Give the position of every P. falciparum parasite, noting its life-cycle stage.
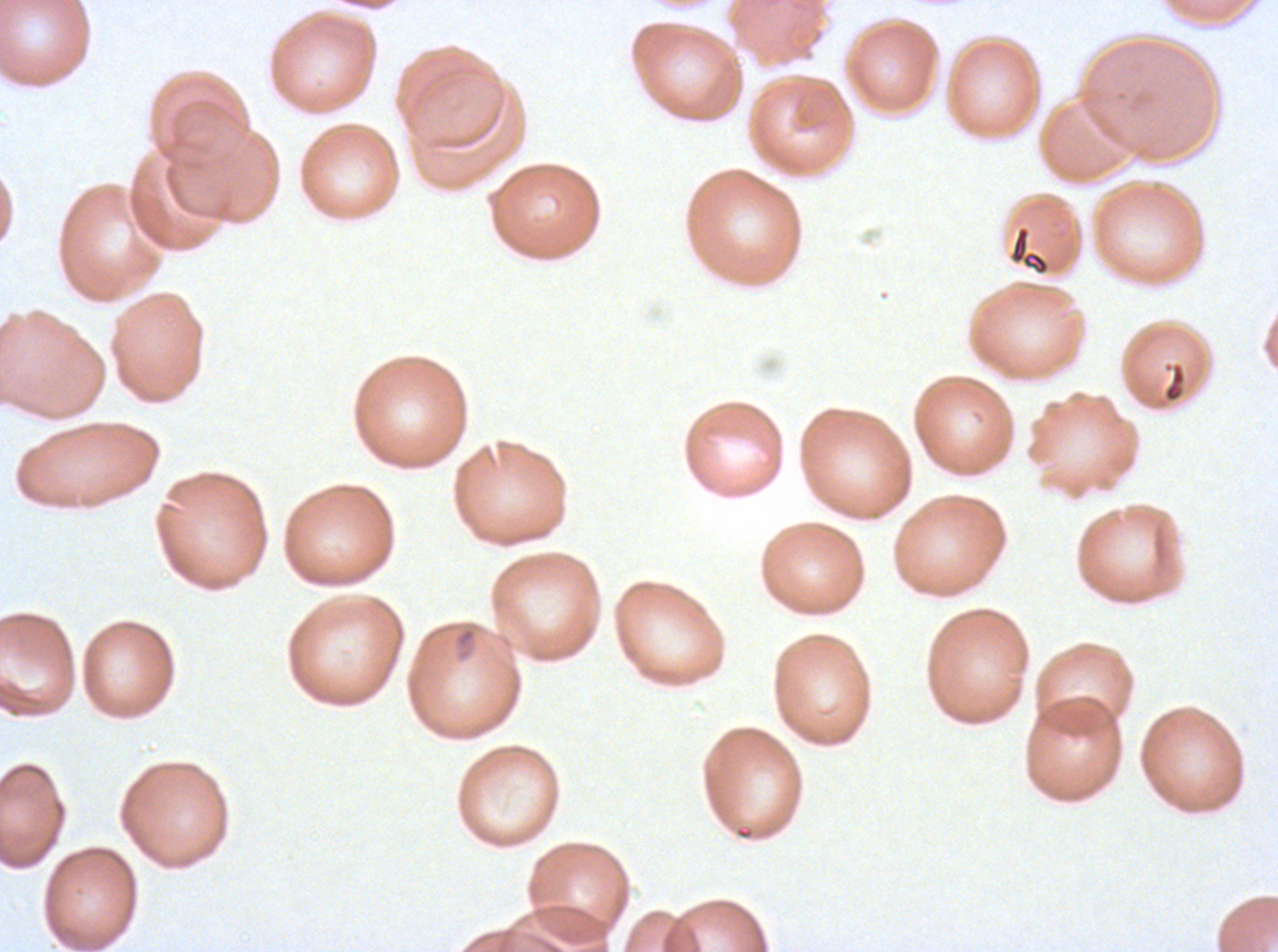

Approximate bounding boxes as (x1, y1, x2, y2) in pixels.
Rings: (453, 626, 478, 662).
No late-ring/early-trophozoite forms, mid trophozoites, late trophozoites, early schizonts, late schizonts, segmenters, or gametocytes observed.

{
  "field_of_view": "one sub-image of a larger composite",
  "image_size": "1278×952 pixels",
  "stain": "Giemsa",
  "debris_locations": "approximate bounding boxes as (x1, y1, x2, y2) in pixels: (1009, 226, 1050, 275), (1162, 360, 1186, 404)",
  "preparation": "thin blood film",
  "specimen": "P. falciparum cultured ex vivo for 24 to 48 hours, from a patient in The Gambia"
}